Assess this cell for malaria.
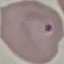
It is parasitized.

Summary:
  - Stain: Giemsa
  - Preparation: thin blood film
  - Capture: smartphone camera at the microscope eyepiece
  - Image type: cell patch, automatically extracted from a larger field of view and resized to 64 × 64 pixels